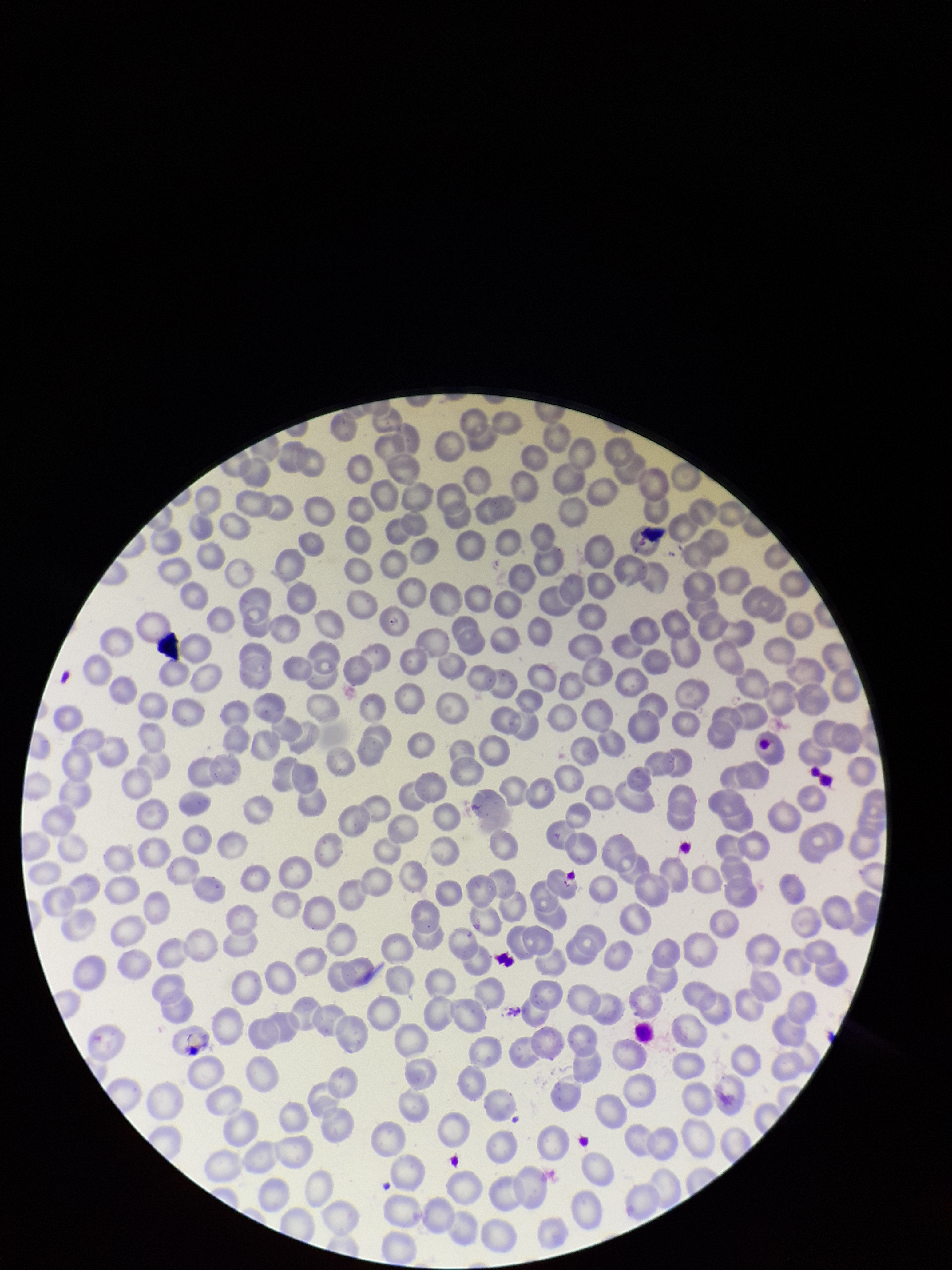

field of view = single
parasitized red blood cells = none seen
parasitized red blood cell count = 0
stain = Giemsa
red blood cell count = 273
patient malaria status = negative
capture = smartphone photograph through the microscope eyepiece
image size = 952×1270 pixels
preparation = thin